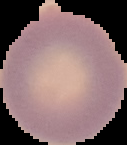
Summary:
  - Image type: cell region segmented out of the field of view; surrounding area masked to black
  - Image size: 127×145 pixels
  - Result: no Plasmodium parasites detected
  - Preparation: thin blood smear